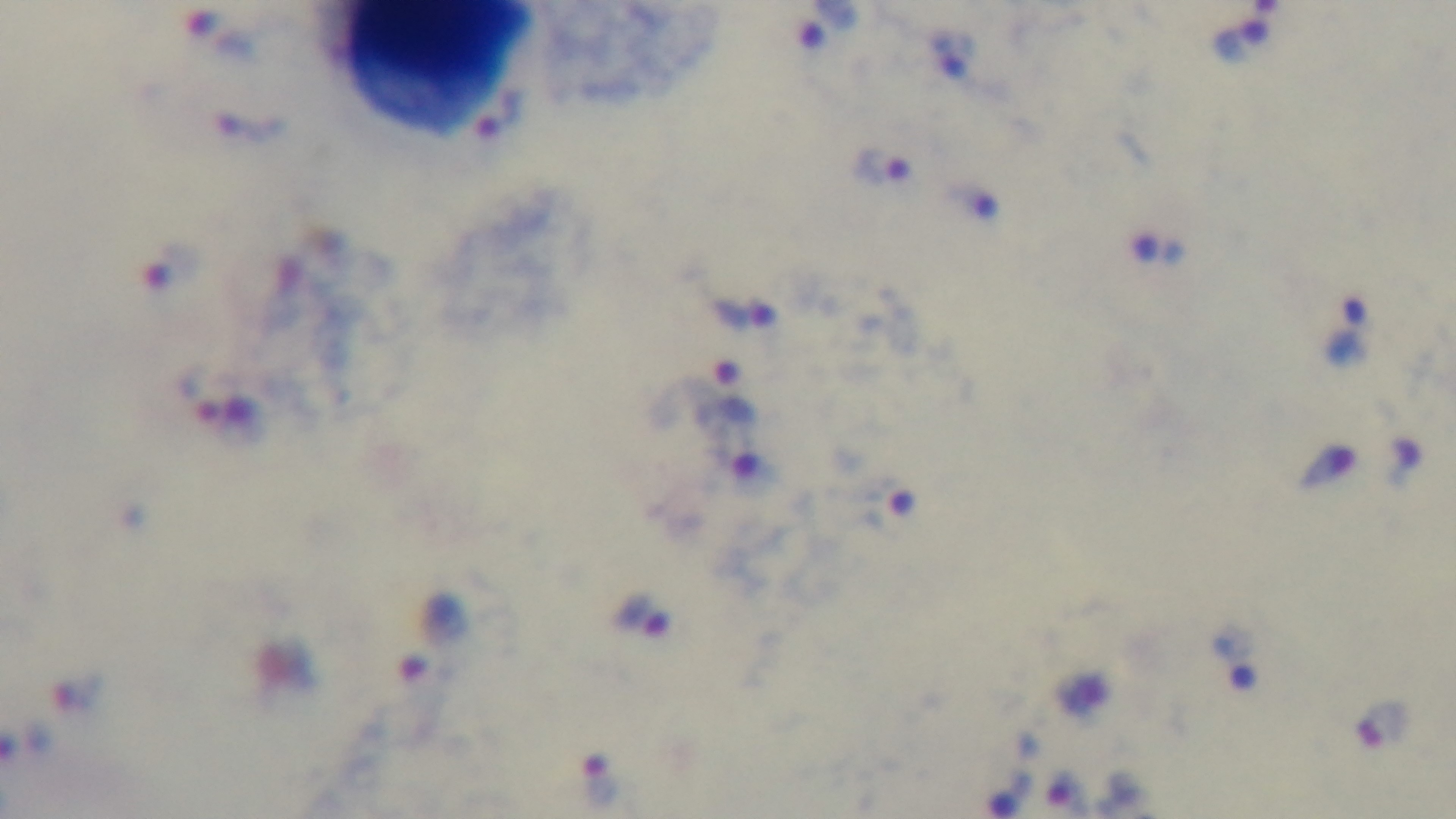
Summary:
  - Preparation: thick smear
  - Field of view: single
  - Modality: light microscopy
  - Stain: Giemsa
  - Objective: 100x oil immersion
  - Malaria status: infected
  - Capture: mounted 4K digital camera